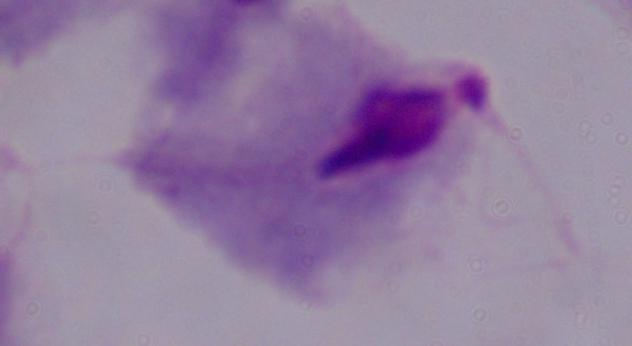

Summary:
  - Magnification: 1000x
  - Modality: micrograph
  - Identification: trichomonad